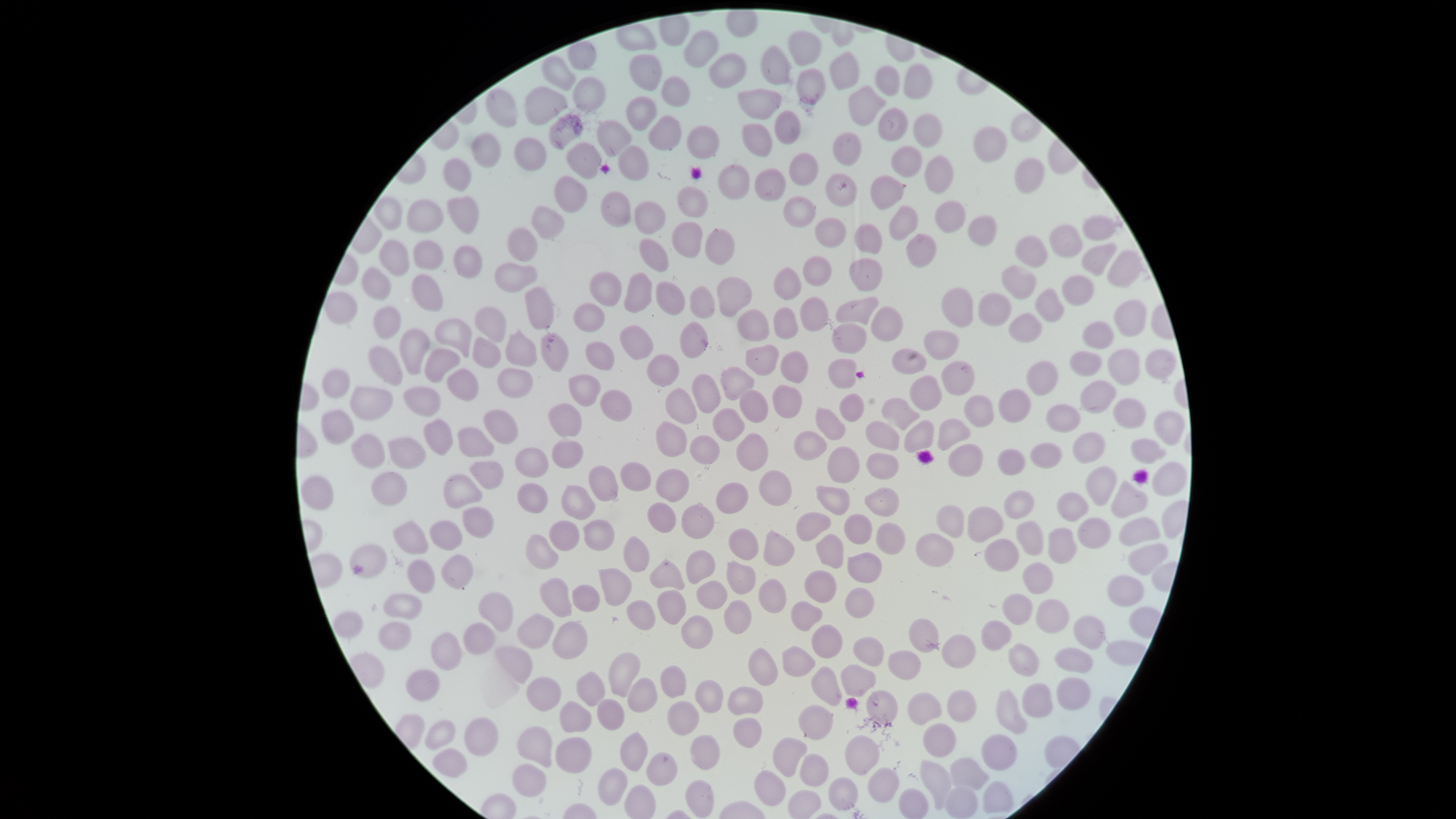
Approximate bounding boxes, in pixels from the top-left corner. Uninfected RBCs: (left=615, top=23, right=657, bottom=51), (left=683, top=29, right=720, bottom=68), (left=787, top=30, right=822, bottom=66), (left=760, top=44, right=791, bottom=85), (left=708, top=51, right=746, bottom=89), (left=829, top=51, right=859, bottom=91), (left=628, top=53, right=663, bottom=91), (left=540, top=55, right=577, bottom=91), (left=903, top=63, right=933, bottom=99), (left=874, top=65, right=900, bottom=97), (left=796, top=68, right=826, bottom=105), (left=660, top=75, right=690, bottom=107), (left=572, top=76, right=607, bottom=112), (left=524, top=85, right=567, bottom=126), (left=847, top=85, right=887, bottom=126), (left=485, top=88, right=518, bottom=128), (left=737, top=88, right=782, bottom=120), (left=626, top=96, right=656, bottom=132), (left=877, top=107, right=908, bottom=142), (left=773, top=109, right=801, bottom=145), (left=912, top=113, right=943, bottom=148), (left=548, top=114, right=584, bottom=150), (left=648, top=114, right=682, bottom=151), (left=596, top=119, right=632, bottom=158), (left=741, top=122, right=773, bottom=157), (left=686, top=125, right=720, bottom=159), (left=973, top=125, right=1007, bottom=163), (left=470, top=132, right=501, bottom=169), (left=832, top=132, right=862, bottom=166), (left=513, top=137, right=547, bottom=172), (left=566, top=142, right=602, bottom=179), (left=617, top=145, right=649, bottom=181), (left=890, top=145, right=923, bottom=177), (left=788, top=152, right=818, bottom=186), (left=924, top=155, right=954, bottom=194), (left=442, top=158, right=472, bottom=191), (left=1014, top=158, right=1045, bottom=195), (left=717, top=163, right=750, bottom=200), (left=754, top=167, right=786, bottom=201), (left=825, top=173, right=857, bottom=207), (left=554, top=174, right=588, bottom=213), (left=870, top=175, right=905, bottom=210), (left=676, top=186, right=709, bottom=217), (left=600, top=190, right=631, bottom=227), (left=446, top=195, right=480, bottom=235), (left=783, top=195, right=816, bottom=228), (left=373, top=196, right=402, bottom=230), (left=405, top=199, right=444, bottom=233), (left=934, top=199, right=966, bottom=234), (left=634, top=200, right=666, bottom=235), (left=530, top=205, right=565, bottom=240), (left=888, top=205, right=919, bottom=240), (left=967, top=215, right=997, bottom=247), (left=1081, top=215, right=1116, bottom=240), (left=814, top=217, right=846, bottom=248), (left=671, top=221, right=703, bottom=259), (left=854, top=223, right=882, bottom=255), (left=1049, top=224, right=1083, bottom=258), (left=506, top=227, right=538, bottom=262), (left=704, top=228, right=735, bottom=265), (left=905, top=233, right=937, bottom=268), (left=1015, top=235, right=1048, bottom=268), (left=638, top=238, right=669, bottom=273), (left=379, top=239, right=410, bottom=277), (left=412, top=240, right=444, bottom=269), (left=1081, top=242, right=1117, bottom=276), (left=451, top=245, right=482, bottom=279), (left=1107, top=249, right=1142, bottom=289), (left=802, top=255, right=832, bottom=287), (left=849, top=257, right=883, bottom=291), (left=494, top=261, right=538, bottom=293), (left=1002, top=265, right=1037, bottom=300), (left=361, top=266, right=391, bottom=301), (left=773, top=267, right=803, bottom=301), (left=589, top=270, right=621, bottom=307), (left=623, top=272, right=652, bottom=313), (left=411, top=274, right=443, bottom=312), (left=1061, top=275, right=1094, bottom=306), (left=716, top=276, right=753, bottom=317), (left=655, top=281, right=686, bottom=315), (left=689, top=285, right=715, bottom=319), (left=524, top=286, right=554, bottom=330), (left=941, top=286, right=973, bottom=328), (left=1034, top=288, right=1065, bottom=323), (left=324, top=290, right=358, bottom=325), (left=977, top=292, right=1012, bottom=327), (left=836, top=296, right=880, bottom=325), (left=800, top=297, right=828, bottom=333), (left=1113, top=299, right=1146, bottom=337), (left=573, top=303, right=605, bottom=333), (left=373, top=305, right=401, bottom=338), (left=474, top=306, right=507, bottom=342), (left=773, top=306, right=799, bottom=340), (left=870, top=306, right=903, bottom=342), (left=736, top=308, right=770, bottom=342), (left=1008, top=313, right=1043, bottom=343), (left=434, top=318, right=472, bottom=357), (left=1081, top=320, right=1114, bottom=349), (left=679, top=321, right=708, bottom=359), (left=831, top=323, right=867, bottom=354), (left=620, top=325, right=653, bottom=360), (left=399, top=328, right=430, bottom=376), (left=504, top=329, right=538, bottom=367), (left=923, top=330, right=960, bottom=361), (left=540, top=332, right=570, bottom=372), (left=471, top=336, right=501, bottom=369), (left=585, top=341, right=615, bottom=371), (left=745, top=344, right=780, bottom=376), (left=368, top=346, right=403, bottom=385), (left=892, top=347, right=927, bottom=375), (left=1108, top=348, right=1140, bottom=386), (left=424, top=349, right=460, bottom=383), (left=1144, top=349, right=1176, bottom=379), (left=1069, top=350, right=1102, bottom=377), (left=780, top=351, right=808, bottom=383), (left=647, top=354, right=679, bottom=387), (left=828, top=358, right=857, bottom=389), (left=941, top=360, right=976, bottom=396), (left=1026, top=361, right=1059, bottom=396), (left=719, top=366, right=754, bottom=401), (left=497, top=367, right=534, bottom=399), (left=322, top=368, right=350, bottom=398), (left=446, top=369, right=479, bottom=402), (left=691, top=373, right=721, bottom=414), (left=568, top=374, right=601, bottom=407), (left=910, top=375, right=942, bottom=411), (left=1080, top=380, right=1117, bottom=414), (left=772, top=384, right=802, bottom=418), (left=349, top=385, right=393, bottom=421), (left=403, top=386, right=441, bottom=417), (left=664, top=387, right=697, bottom=424), (left=998, top=388, right=1031, bottom=422), (left=600, top=389, right=633, bottom=422), (left=738, top=389, right=769, bottom=423), (left=839, top=393, right=865, bottom=422), (left=963, top=394, right=995, bottom=427), (left=881, top=397, right=920, bottom=430), (left=1113, top=398, right=1146, bottom=430), (left=547, top=403, right=582, bottom=438), (left=1045, top=403, right=1081, bottom=433), (left=815, top=406, right=846, bottom=440), (left=712, top=408, right=745, bottom=441), (left=320, top=409, right=354, bottom=445), (left=483, top=409, right=518, bottom=444), (left=1153, top=410, right=1185, bottom=446), (left=423, top=418, right=454, bottom=456), (left=937, top=418, right=971, bottom=450), (left=903, top=419, right=934, bottom=453), (left=656, top=421, right=688, bottom=457), (left=864, top=421, right=900, bottom=451), (left=457, top=427, right=495, bottom=457), (left=793, top=430, right=827, bottom=461), (left=351, top=432, right=385, bottom=469), (left=1072, top=432, right=1105, bottom=464), (left=736, top=433, right=769, bottom=471), (left=689, top=435, right=721, bottom=465), (left=388, top=437, right=427, bottom=470), (left=1130, top=438, right=1167, bottom=465), (left=551, top=440, right=583, bottom=469), (left=1029, top=442, right=1062, bottom=469), (left=947, top=443, right=984, bottom=477), (left=827, top=445, right=860, bottom=484), (left=514, top=446, right=549, bottom=478), (left=997, top=448, right=1026, bottom=476), (left=865, top=452, right=899, bottom=480), (left=469, top=461, right=504, bottom=490), (left=620, top=461, right=651, bottom=491), (left=1151, top=461, right=1187, bottom=497), (left=588, top=465, right=619, bottom=502), (left=1084, top=465, right=1117, bottom=506), (left=655, top=469, right=690, bottom=502), (left=758, top=470, right=792, bottom=506), (left=371, top=471, right=408, bottom=506), (left=443, top=473, right=482, bottom=509), (left=300, top=474, right=334, bottom=512), (left=1110, top=479, right=1148, bottom=518), (left=517, top=482, right=548, bottom=514), (left=715, top=482, right=749, bottom=514), (left=561, top=485, right=595, bottom=520), (left=815, top=485, right=850, bottom=515), (left=865, top=487, right=900, bottom=517), (left=1003, top=490, right=1034, bottom=520), (left=1056, top=492, right=1089, bottom=523), (left=647, top=501, right=677, bottom=533), (left=680, top=503, right=715, bottom=540), (left=935, top=504, right=965, bottom=538), (left=462, top=507, right=494, bottom=539), (left=967, top=507, right=1004, bottom=543), (left=795, top=512, right=832, bottom=541), (left=844, top=513, right=873, bottom=544), (left=1118, top=516, right=1161, bottom=547), (left=1077, top=517, right=1111, bottom=549), (left=582, top=519, right=615, bottom=551), (left=392, top=520, right=429, bottom=555), (left=429, top=520, right=463, bottom=550), (left=549, top=520, right=580, bottom=551), (left=1016, top=520, right=1043, bottom=556), (left=875, top=522, right=906, bottom=554), (left=728, top=528, right=759, bottom=561), (left=1047, top=528, right=1078, bottom=564), (left=763, top=530, right=795, bottom=567), (left=915, top=532, right=955, bottom=567), (left=816, top=533, right=844, bottom=569), (left=525, top=534, right=559, bottom=570), (left=623, top=536, right=650, bottom=573), (left=983, top=538, right=1019, bottom=572), (left=1127, top=542, right=1169, bottom=576), (left=349, top=543, right=388, bottom=579), (left=686, top=550, right=716, bottom=584), (left=846, top=552, right=882, bottom=583), (left=441, top=554, right=473, bottom=590), (left=649, top=558, right=685, bottom=590), (left=406, top=559, right=435, bottom=594), (left=727, top=559, right=756, bottom=595), (left=1021, top=562, right=1054, bottom=594), (left=598, top=568, right=632, bottom=607), (left=804, top=569, right=837, bottom=603), (left=1106, top=575, right=1145, bottom=607), (left=540, top=578, right=573, bottom=617), (left=758, top=578, right=786, bottom=613), (left=696, top=580, right=728, bottom=610), (left=571, top=584, right=601, bottom=613), (left=844, top=587, right=875, bottom=619), (left=657, top=589, right=687, bottom=625), (left=477, top=592, right=513, bottom=632), (left=382, top=593, right=423, bottom=620), (left=1001, top=593, right=1034, bottom=625), (left=723, top=599, right=752, bottom=634), (left=1035, top=599, right=1070, bottom=634), (left=626, top=600, right=655, bottom=631), (left=790, top=601, right=823, bottom=632), (left=332, top=610, right=364, bottom=639), (left=517, top=614, right=554, bottom=649), (left=680, top=614, right=713, bottom=649), (left=1072, top=615, right=1105, bottom=649), (left=908, top=618, right=939, bottom=653), (left=551, top=620, right=588, bottom=659), (left=981, top=620, right=1012, bottom=651), (left=377, top=622, right=412, bottom=651), (left=463, top=622, right=496, bottom=654), (left=811, top=624, right=843, bottom=658), (left=430, top=632, right=462, bottom=671), (left=941, top=634, right=976, bottom=668), (left=853, top=636, right=885, bottom=667), (left=1008, top=643, right=1040, bottom=677), (left=782, top=645, right=815, bottom=677), (left=495, top=646, right=533, bottom=684), (left=748, top=647, right=778, bottom=686), (left=1053, top=648, right=1094, bottom=673), (left=888, top=650, right=921, bottom=681), (left=608, top=653, right=641, bottom=698), (left=840, top=664, right=876, bottom=697), (left=659, top=665, right=687, bottom=698), (left=811, top=666, right=843, bottom=707), (left=405, top=668, right=441, bottom=702), (left=576, top=671, right=606, bottom=706), (left=526, top=676, right=561, bottom=711), (left=1055, top=676, right=1091, bottom=711), (left=627, top=677, right=658, bottom=713), (left=694, top=680, right=723, bottom=713), (left=1021, top=683, right=1053, bottom=718), (left=727, top=686, right=763, bottom=716), (left=865, top=689, right=899, bottom=724), (left=946, top=689, right=977, bottom=722), (left=995, top=690, right=1028, bottom=734), (left=907, top=692, right=942, bottom=725), (left=596, top=698, right=625, bottom=731), (left=559, top=700, right=592, bottom=732), (left=666, top=700, right=700, bottom=736), (left=798, top=704, right=834, bottom=741), (left=464, top=717, right=498, bottom=756), (left=732, top=717, right=763, bottom=748), (left=424, top=719, right=456, bottom=750), (left=922, top=722, right=957, bottom=758), (left=516, top=726, right=553, bottom=768), (left=619, top=731, right=648, bottom=772), (left=690, top=734, right=720, bottom=770), (left=981, top=734, right=1017, bottom=771), (left=844, top=735, right=880, bottom=775), (left=555, top=736, right=593, bottom=773), (left=772, top=737, right=808, bottom=777), (left=432, top=748, right=467, bottom=778), (left=646, top=752, right=678, bottom=786), (left=799, top=753, right=829, bottom=787), (left=949, top=757, right=989, bottom=790), (left=919, top=760, right=952, bottom=810), (left=511, top=763, right=546, bottom=797), (left=598, top=767, right=628, bottom=806), (left=868, top=767, right=900, bottom=803), (left=754, top=770, right=786, bottom=806), (left=828, top=776, right=859, bottom=810), (left=685, top=779, right=715, bottom=818), (left=944, top=786, right=978, bottom=818), (left=898, top=788, right=929, bottom=819), (left=787, top=789, right=822, bottom=819). Circular visible region. Smartphone photograph through the microscope eyepiece. Giemsa stain. Presence: no malaria parasites detected. Thin blood smear. One field of view of the specimen. Image is 1456×819 pixels.